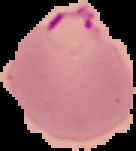

malaria status = parasitized
image type = segmented cell region on a black background
image size = 136×151 pixels
preparation = thin blood film